Describe the morphology of the erythrocytes.
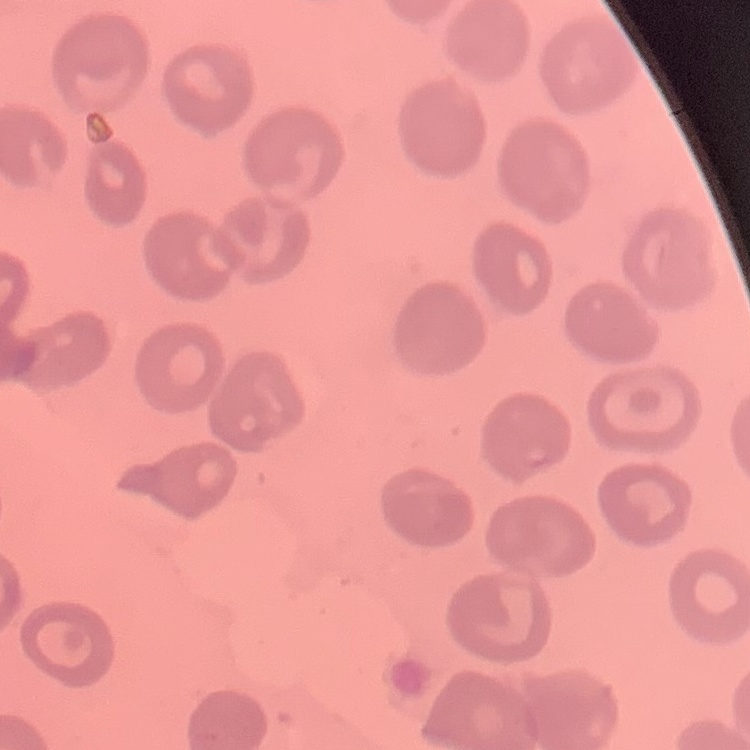

They show no rouleaux formation.

stain = Field's or Giemsa
image type = one tile cut from a larger photomicrograph
preparation = thin blood smear